Classify this cell by malaria status.
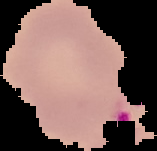
Parasitized.

preparation = thin blood smear
image size = 157×151 pixels
image type = segmented cell region with the area outside set to black